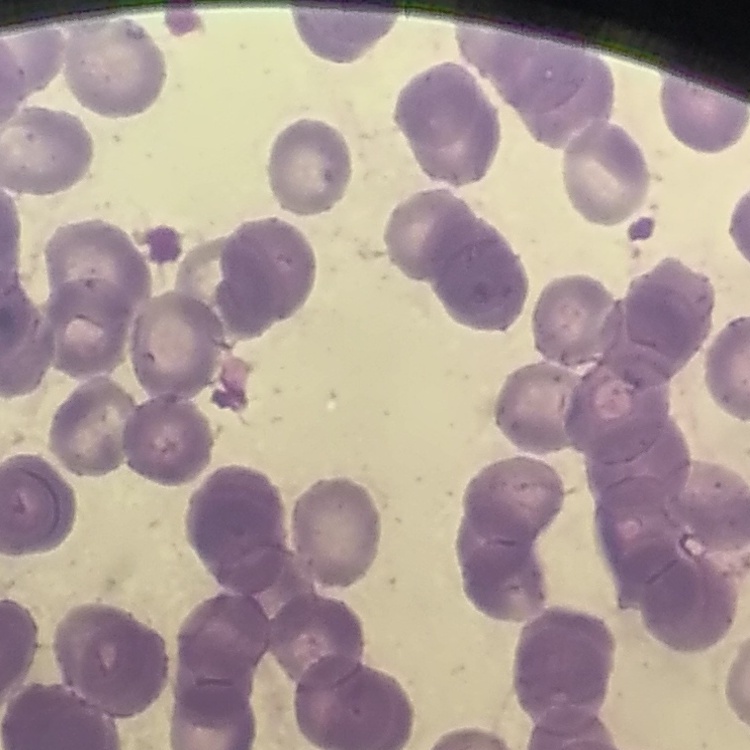
Summary:
  - Red blood cell morphology: rouleaux formation
  - Image type: one tile cut from a larger photomicrograph
  - Stain: Field's or Giemsa
  - Preparation: thin blood film